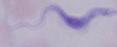

Captured at 1000x magnification. A trypanosome is seen. Photomicrograph.